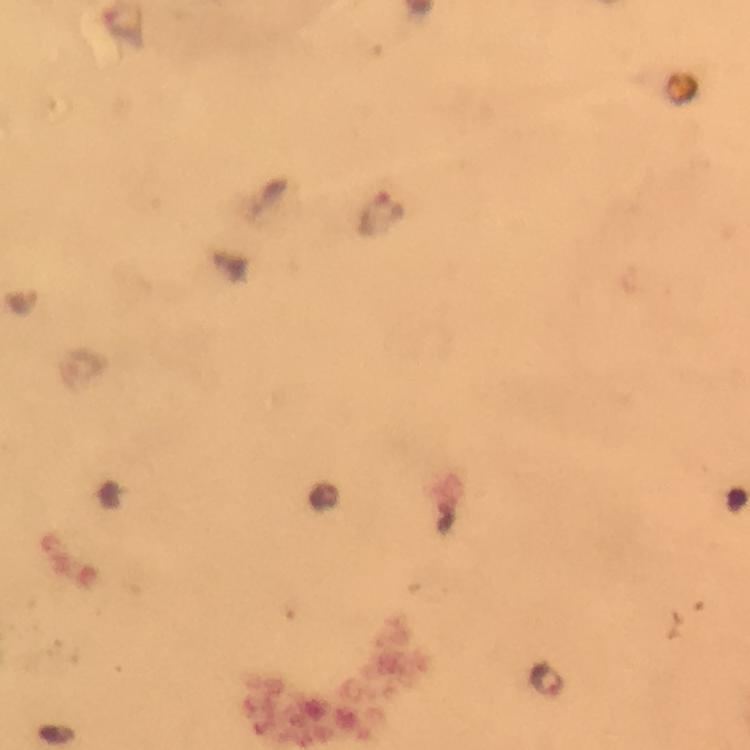

Approximate centers as [x, y] in pixels.
Summary:
  - Plasmodium parasite locations: [380, 213], [547, 679]
  - Capture: smartphone mounted on the microscope
  - Preparation: thick smear
  - Magnification: 100x
  - Immersion oil: used
  - Context: from a malaria diagnostic workup
  - Image size: 750×750 pixels
  - Stain: Giemsa
  - Cropped from: one field of view